State which parasite is depicted.
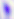
Toxoplasma gondii.

Summary:
  - Magnification: 400x
  - Modality: photomicrograph